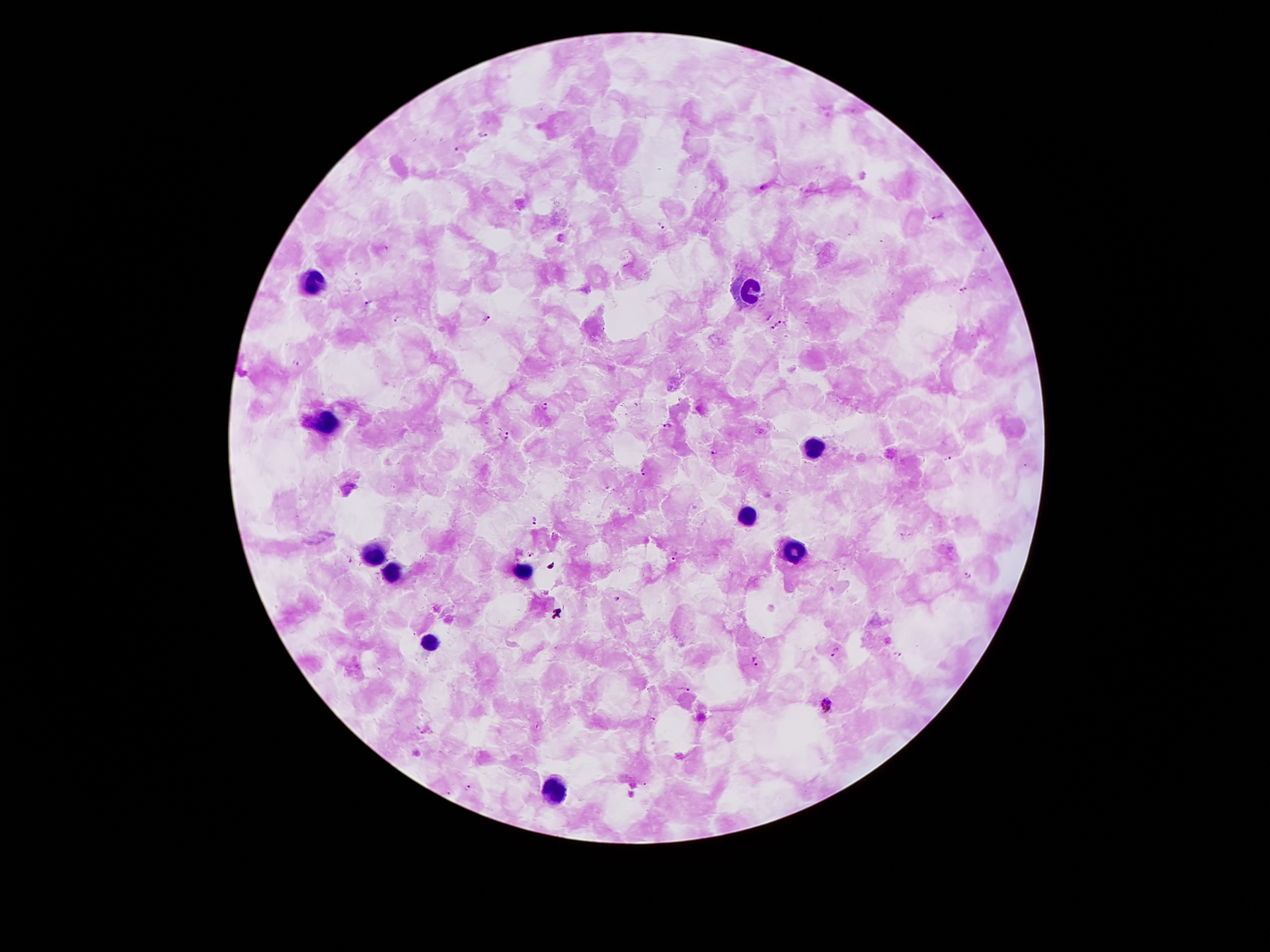
{
  "field_of_view": "single",
  "malaria_parasite_locations": "approximate object centers, in pixels from the top-left corner: (x=483, y=134), (x=458, y=150), (x=940, y=216), (x=663, y=227), (x=964, y=289), (x=368, y=300), (x=398, y=318), (x=489, y=320), (x=786, y=320), (x=776, y=325), (x=296, y=363), (x=546, y=407), (x=668, y=426), (x=507, y=436), (x=714, y=451), (x=948, y=459), (x=645, y=471), (x=534, y=519), (x=531, y=553), (x=676, y=556), (x=968, y=577), (x=618, y=597), (x=836, y=653), (x=899, y=653), (x=758, y=660), (x=686, y=689), (x=827, y=703), (x=652, y=719), (x=424, y=731), (x=468, y=788)",
  "leukocyte_locations": "approximate object centers, in pixels from the top-left corner: (x=313, y=281), (x=748, y=288), (x=324, y=422), (x=815, y=449), (x=748, y=519), (x=792, y=548), (x=377, y=553), (x=393, y=571), (x=525, y=573), (x=430, y=640), (x=554, y=792)",
  "capture": "smartphone through the microscope eyepiece",
  "preparation": "thick peripheral-blood smear",
  "magnification": "100x",
  "image_size": "1270×952 pixels",
  "patient_malaria_status": "positive for Plasmodium falciparum",
  "stain": "Giemsa"
}